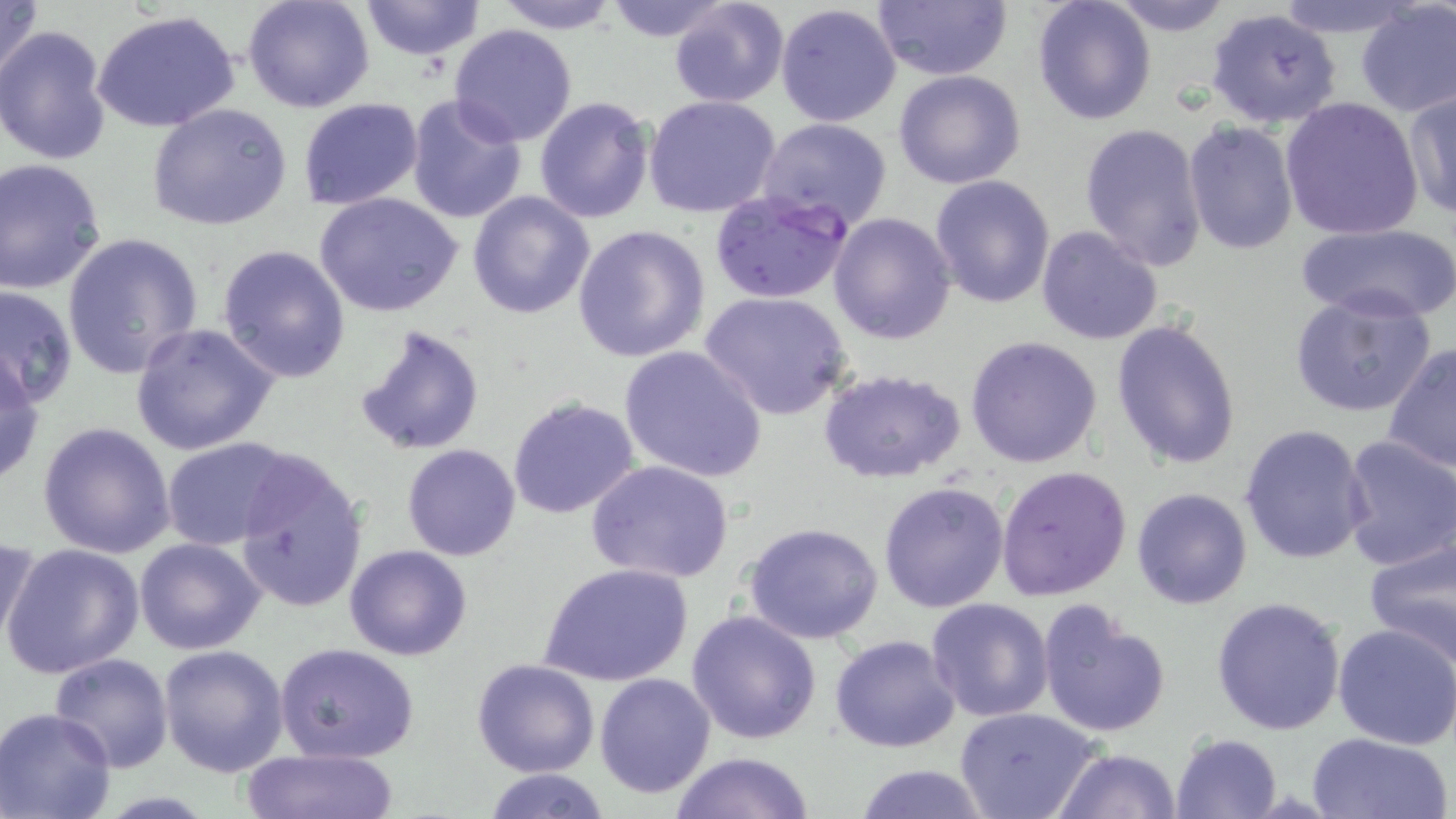
Summary:
  - Coordinate format: approximate bounding boxes as (x1,y1)-(x2,y2) corner pairs in pixels
  - Uninfected red blood cell locations: (0,0)-(45,91), (242,0)-(376,112), (357,0)-(486,60), (489,0)-(623,34), (599,0)-(738,42), (666,0)-(789,109), (868,0)-(1012,82), (1031,0)-(1158,126), (1104,0)-(1237,37), (1269,0)-(1421,38), (1354,2)-(1456,119), (775,3)-(902,127), (1206,7)-(1345,129), (93,11)-(241,132), (1,24)-(116,165), (448,24)-(579,147), (893,68)-(1026,189), (1402,87)-(1456,221), (405,93)-(529,227), (643,94)-(781,217), (534,96)-(655,223), (297,98)-(423,209), (1278,99)-(1425,240), (147,102)-(295,233), (758,118)-(893,231), (1183,120)-(1300,256), (1079,122)-(1208,271), (0,161)-(107,293), (929,175)-(1055,309), (468,189)-(596,320), (314,193)-(464,318), (829,211)-(957,344), (572,223)-(712,362), (1297,223)-(1456,323), (1036,225)-(1164,347), (62,231)-(204,380), (216,243)-(350,383), (0,285)-(77,410), (1288,289)-(1437,418), (700,291)-(853,419), (1112,319)-(1242,472), (131,322)-(280,456), (355,324)-(485,456), (965,335)-(1103,469), (1385,343)-(1455,478), (618,345)-(768,482), (0,352)-(45,486), (817,367)-(967,484), (507,396)-(640,519), (38,421)-(177,559), (1239,424)-(1370,565), (1340,436)-(1456,571), (164,438)-(298,550), (402,444)-(521,562), (230,449)-(369,612), (586,459)-(736,587), (995,464)-(1132,601), (878,480)-(1010,614), (1132,487)-(1252,609), (744,524)-(883,644), (1361,529)-(1456,668), (0,532)-(42,657), (134,536)-(266,654), (1,543)-(145,680), (344,545)-(473,661), (538,561)-(694,687), (1210,596)-(1346,737), (926,597)-(1055,721), (1035,601)-(1171,739), (686,608)-(821,744), (1333,624)-(1456,749), (831,633)-(961,752), (275,642)-(421,763), (159,644)-(289,777), (49,653)-(174,773), (471,657)-(600,777), (594,671)-(716,799), (955,708)-(1102,819), (0,709)-(119,819), (1304,731)-(1452,819), (1170,733)-(1281,819), (1054,746)-(1181,819), (241,748)-(400,819), (669,751)-(816,819), (852,763)-(992,819), (484,768)-(611,819)
  - Plasmodium falciparum-infected red blood cell locations: (709,191)-(854,306)
  - Slide-level diagnosis: Plasmodium falciparum
  - Magnification: 1000x
  - Modality: optical microscopy
  - Stain: May-Grünwald-Giemsa
  - Field of view: single
  - Preparation: thin blood smear
  - Image size: 1456×819 pixels